Report the malaria status of this cell.
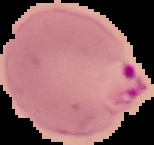

Parasitized.

Summary:
  - Image size: 154×145 pixels
  - Preparation: thin blood film
  - Image type: segmented cell region with the area outside set to black